Classify this cell by malaria status.
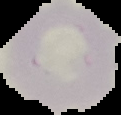

It is uninfected.

preparation: thin blood smear
image_type: cell region segmented out of the field of view; surrounding area masked to black
image_size: 121×115 pixels